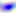 400x magnification. Micrograph. Toxoplasma gondii is shown.